Locate every Plasmodium ovale-infected red blood cell.
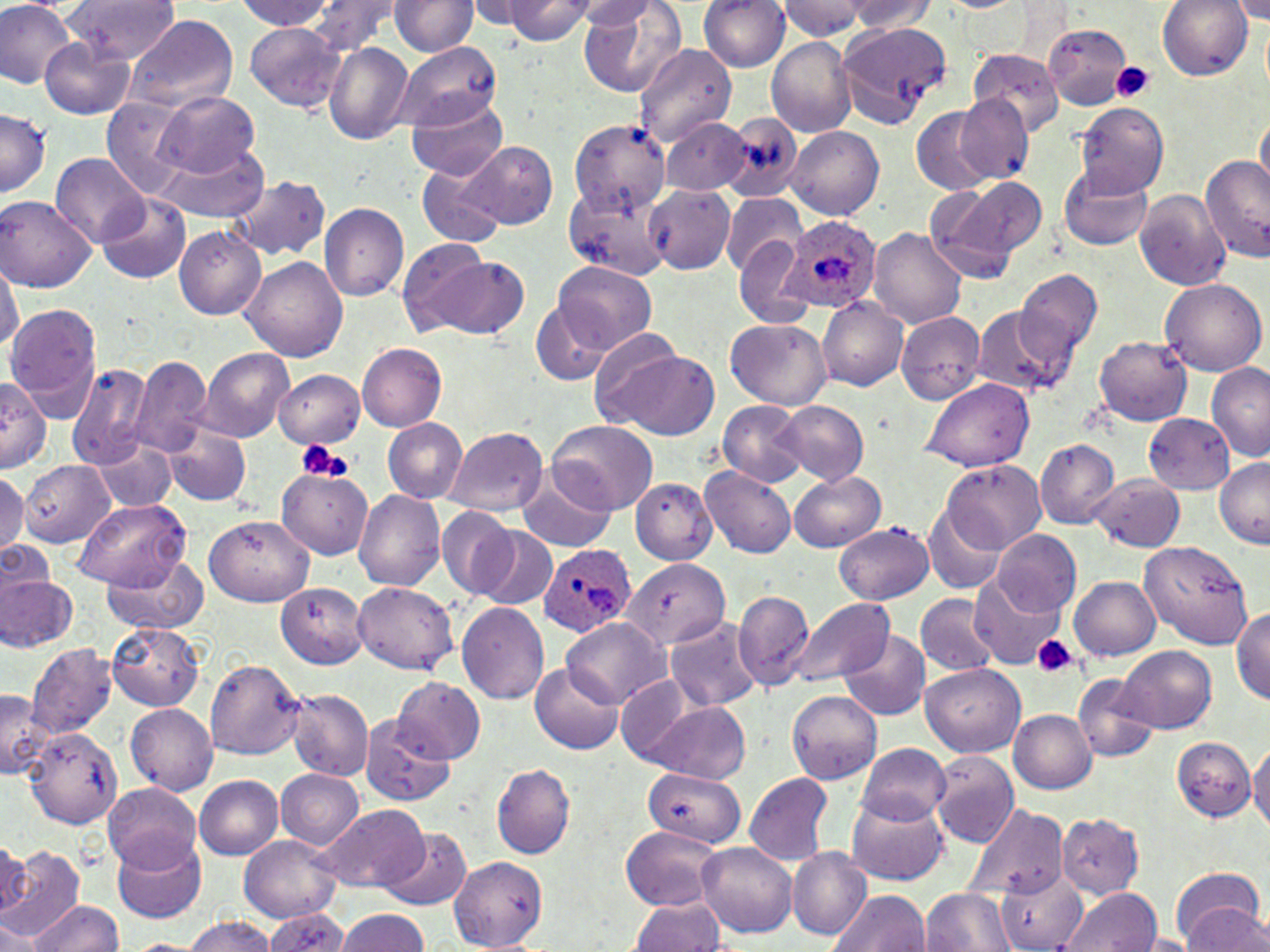
Approximate bounding boxes as [x1, y1, x2, y2] in pixels.
Plasmodium ovale-infected red blood cells: [782, 214, 882, 309], [538, 541, 636, 638].

slide-level diagnosis = Plasmodium ovale
image size = 1270×952 pixels
uninfected red blood cell locations = approximate bounding boxes as [x1, y1, x2, y2] in pixels: [62, 0, 182, 62], [236, 0, 346, 32], [304, 0, 402, 52], [392, 0, 476, 56], [468, 0, 534, 31], [500, 0, 596, 44], [569, 0, 657, 27], [575, 0, 691, 96], [699, 0, 789, 73], [781, 0, 868, 40], [844, 0, 936, 34], [1155, 0, 1255, 81], [1233, 0, 1270, 23], [0, 1, 78, 88], [126, 14, 238, 115], [1041, 21, 1133, 106], [244, 23, 346, 113], [838, 23, 951, 128], [40, 34, 135, 118], [768, 37, 856, 137], [324, 41, 413, 144], [394, 41, 501, 130], [635, 43, 738, 144], [967, 47, 1066, 143], [971, 52, 1063, 135], [154, 90, 260, 179], [407, 90, 511, 179], [956, 95, 1034, 184], [103, 102, 192, 197], [1076, 103, 1168, 194], [909, 104, 1005, 194], [722, 110, 804, 201], [1253, 111, 1269, 183], [0, 112, 49, 197], [569, 119, 669, 215], [663, 120, 750, 197], [788, 128, 882, 220], [159, 141, 268, 221], [456, 141, 561, 230], [1199, 155, 1269, 264], [53, 156, 149, 250], [414, 163, 509, 246], [1058, 166, 1154, 249], [224, 174, 332, 262], [925, 176, 1045, 283], [645, 186, 734, 274], [1132, 188, 1232, 292], [98, 193, 190, 283], [722, 194, 804, 275], [0, 196, 98, 292], [320, 204, 410, 301], [868, 226, 968, 329], [174, 228, 266, 319], [734, 239, 813, 326], [399, 246, 531, 344], [242, 255, 347, 363], [1, 257, 21, 369], [552, 262, 658, 354], [1010, 267, 1102, 375], [1160, 279, 1266, 377], [818, 299, 909, 389], [7, 303, 102, 422], [532, 304, 615, 386], [971, 305, 1066, 395], [897, 313, 985, 404], [727, 321, 832, 409], [1092, 332, 1195, 425], [592, 343, 720, 438], [358, 345, 447, 430], [199, 347, 295, 441], [130, 358, 211, 460], [67, 362, 152, 465], [1206, 362, 1270, 460], [274, 368, 366, 449], [0, 376, 48, 474], [923, 380, 1033, 471], [718, 400, 807, 485], [775, 401, 868, 484], [1143, 413, 1236, 493], [381, 419, 465, 503], [547, 421, 660, 513], [166, 425, 249, 505], [447, 428, 549, 514], [93, 439, 175, 514], [1035, 440, 1118, 527], [1214, 457, 1269, 549], [19, 459, 118, 549], [941, 461, 1045, 550], [278, 466, 374, 559], [701, 467, 795, 558], [788, 469, 887, 551], [0, 472, 27, 553], [1089, 473, 1184, 551], [633, 475, 716, 563], [517, 478, 618, 551], [354, 490, 445, 591], [74, 499, 192, 590], [925, 506, 1009, 593], [437, 510, 519, 596], [203, 515, 312, 605], [834, 523, 936, 604], [471, 525, 559, 611], [995, 529, 1080, 616], [1141, 539, 1255, 649], [3, 540, 54, 603], [102, 549, 210, 633], [619, 555, 731, 653], [971, 571, 1061, 664], [0, 576, 78, 652], [1069, 576, 1162, 660], [354, 580, 458, 675], [276, 581, 368, 669], [735, 589, 814, 691], [915, 592, 998, 677], [793, 598, 896, 684], [457, 602, 550, 704], [1230, 603, 1270, 703], [562, 618, 668, 710], [666, 618, 760, 713], [106, 619, 202, 710], [838, 630, 930, 719], [1118, 644, 1217, 735], [30, 645, 114, 737], [205, 658, 306, 761], [529, 662, 625, 753], [922, 663, 1025, 754], [1073, 675, 1157, 761], [391, 678, 485, 763], [287, 688, 371, 780], [786, 689, 883, 782], [0, 690, 47, 777], [638, 702, 755, 781], [125, 703, 217, 794], [1010, 708, 1098, 794], [359, 716, 453, 805], [21, 727, 121, 829], [1167, 736, 1255, 823], [1251, 741, 1270, 840], [858, 744, 953, 823], [932, 755, 1018, 847], [492, 764, 576, 859], [277, 770, 364, 850], [643, 770, 744, 846], [744, 774, 834, 866], [197, 775, 285, 861], [103, 782, 200, 870], [846, 786, 951, 886], [964, 805, 1065, 899], [322, 806, 430, 892], [1056, 813, 1144, 898], [618, 823, 726, 908], [380, 826, 471, 910], [240, 832, 344, 922], [111, 835, 208, 922], [0, 837, 29, 919], [696, 844, 798, 938], [2, 846, 86, 946], [788, 850, 873, 938], [448, 856, 549, 949], [998, 868, 1088, 952], [1169, 874, 1269, 952], [919, 887, 1018, 952], [828, 888, 929, 952], [1058, 888, 1158, 952], [629, 895, 724, 952], [25, 898, 124, 952], [264, 907, 352, 952], [335, 908, 434, 952], [0, 910, 47, 952], [181, 917, 284, 952], [1141, 933, 1191, 952], [123, 936, 212, 951]
modality = light microscopy
stain = May-Grünwald-Giemsa
magnification = 1000x
field of view = one of a larger specimen
platelet locations = approximate bounding boxes as [x1, y1, x2, y2] in pixels: [1111, 61, 1156, 103], [293, 442, 349, 480], [1033, 634, 1076, 678]
preparation = thin blood smear